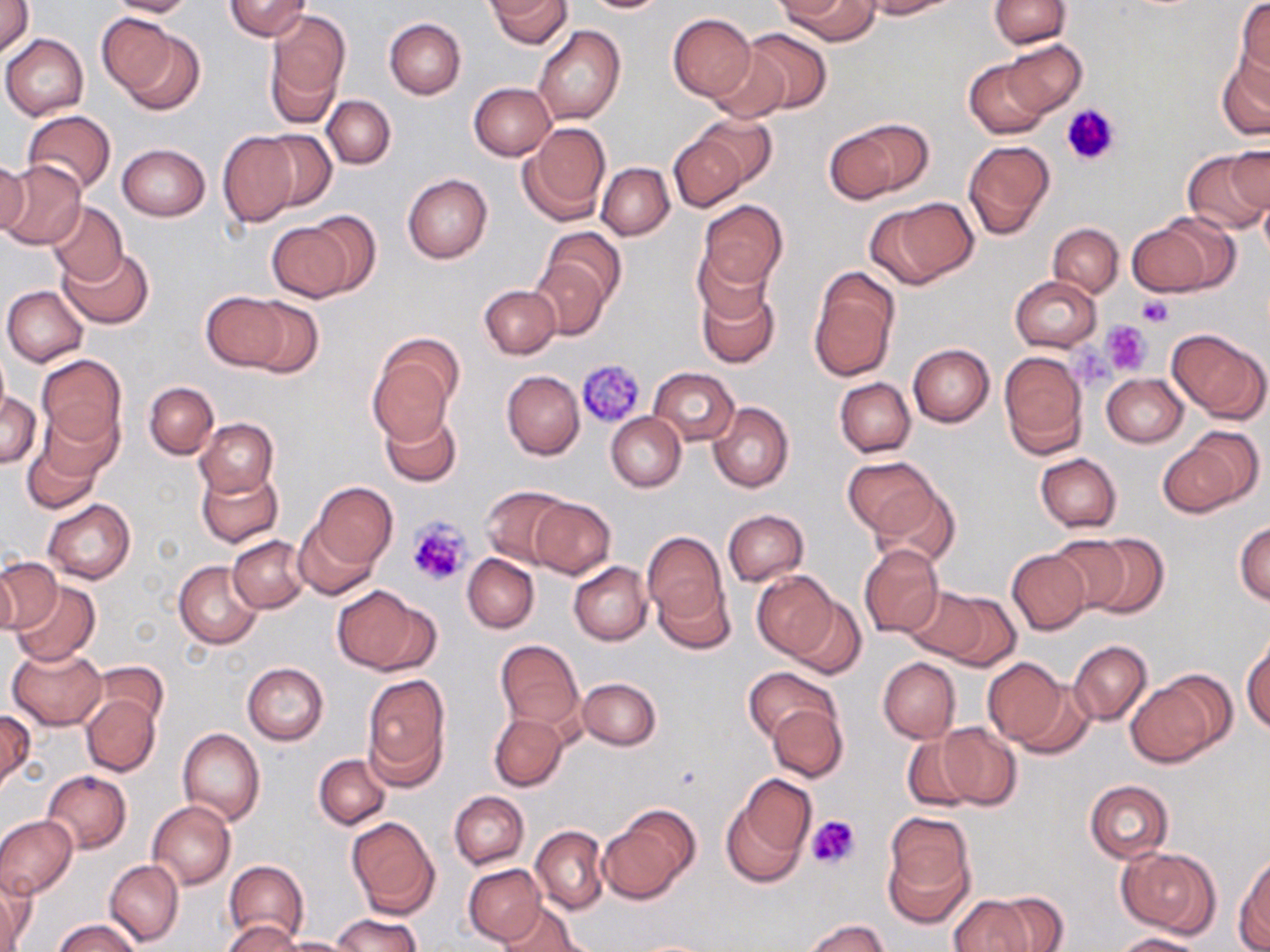
slide-level diagnosis = negative for blood parasites
stain = May-Grünwald-Giemsa
uninfected red blood cell locations = approximate bounding boxes as (x1, y1, x2, y2) in pixels: (105, 0, 196, 17), (225, 0, 312, 41), (489, 0, 573, 49), (580, 0, 672, 13), (862, 0, 957, 18), (989, 0, 1070, 48), (0, 1, 34, 57), (780, 1, 879, 46), (1237, 2, 1270, 78), (265, 8, 350, 122), (988, 10, 1076, 88), (668, 13, 756, 102), (99, 14, 185, 100), (384, 19, 465, 99), (533, 25, 625, 125), (740, 28, 832, 113), (1, 34, 89, 120), (1001, 39, 1087, 117), (707, 49, 789, 123), (1216, 51, 1270, 139), (964, 58, 1049, 138), (468, 83, 555, 160), (322, 94, 395, 168), (22, 111, 116, 196), (692, 114, 776, 187), (826, 118, 933, 202), (520, 121, 612, 222), (256, 131, 336, 211), (216, 132, 298, 227), (670, 134, 748, 212), (963, 141, 1056, 241), (116, 144, 210, 221), (1227, 146, 1269, 215), (1183, 149, 1269, 234), (0, 157, 31, 237), (0, 158, 87, 249), (597, 162, 674, 240), (403, 174, 492, 263), (1259, 192, 1270, 266), (871, 197, 977, 287), (698, 200, 787, 294), (48, 202, 128, 285), (300, 211, 381, 296), (1147, 212, 1241, 293), (265, 221, 357, 301), (1048, 223, 1123, 297), (540, 227, 627, 310), (60, 247, 153, 328), (529, 260, 609, 340), (808, 268, 899, 381), (1010, 276, 1102, 351), (696, 277, 780, 369), (480, 284, 560, 359), (2, 285, 88, 366), (201, 291, 290, 370), (241, 298, 324, 378), (1167, 329, 1269, 423), (908, 343, 994, 427), (368, 347, 459, 443), (0, 349, 10, 426), (999, 351, 1088, 458), (36, 353, 125, 447), (649, 368, 739, 445), (502, 370, 583, 461), (1102, 374, 1187, 447), (836, 378, 915, 457), (143, 381, 218, 459), (0, 392, 42, 469), (709, 401, 794, 493), (379, 407, 461, 486), (34, 408, 121, 491), (606, 412, 686, 491), (195, 418, 279, 497), (1165, 427, 1262, 516), (22, 437, 104, 515), (1035, 453, 1121, 532), (844, 458, 939, 536), (197, 467, 282, 548), (312, 482, 397, 570), (480, 485, 574, 569), (871, 486, 960, 569), (528, 497, 615, 579), (43, 500, 135, 584), (723, 510, 809, 586), (295, 517, 380, 598), (1234, 521, 1270, 605), (642, 530, 730, 633), (1078, 533, 1168, 619), (1049, 534, 1131, 612), (228, 535, 308, 612), (860, 544, 943, 638), (1007, 551, 1090, 634), (463, 554, 539, 632), (0, 558, 61, 635), (0, 560, 19, 635), (174, 561, 264, 648), (569, 562, 652, 645), (650, 571, 735, 654), (753, 572, 837, 658), (12, 580, 100, 666), (332, 586, 433, 675), (902, 588, 990, 661), (931, 589, 1021, 670), (787, 595, 867, 680), (1242, 638, 1270, 734), (495, 639, 584, 731), (1068, 639, 1152, 725), (8, 646, 107, 729), (981, 656, 1070, 747), (877, 657, 960, 744), (242, 662, 329, 745), (94, 663, 167, 731), (743, 667, 841, 745), (1127, 673, 1232, 768), (362, 674, 450, 784), (577, 676, 661, 751), (1006, 676, 1096, 759), (82, 695, 160, 776), (767, 703, 847, 782), (0, 710, 34, 792), (489, 713, 567, 791), (936, 723, 1022, 810), (177, 728, 265, 826), (901, 733, 982, 813), (314, 753, 391, 830), (41, 771, 132, 853), (722, 776, 814, 886), (1085, 780, 1175, 863), (449, 791, 528, 868), (148, 801, 235, 888), (599, 808, 698, 903), (882, 813, 976, 922), (0, 815, 76, 899), (347, 818, 438, 917), (531, 825, 609, 914), (1118, 845, 1220, 938), (1236, 856, 1270, 948), (106, 858, 184, 946), (224, 859, 308, 946), (463, 864, 545, 946), (2, 871, 34, 952), (986, 891, 1068, 951), (947, 895, 1036, 952), (496, 902, 586, 952), (332, 914, 421, 952), (805, 918, 889, 952), (54, 919, 139, 952), (224, 919, 302, 951), (1116, 932, 1207, 952), (276, 936, 356, 951)
platelet locations = approximate bounding boxes as (x1, y1, x2, y2) in pixels: (1062, 104, 1120, 167), (1135, 294, 1175, 329), (1102, 320, 1152, 375), (1068, 339, 1114, 393), (576, 357, 644, 426), (406, 517, 471, 586), (805, 815, 861, 871)
preparation = thin blood smear
image size = 1270×952 pixels
modality = light microscopy
magnification = 1000x
field of view = one of a larger specimen